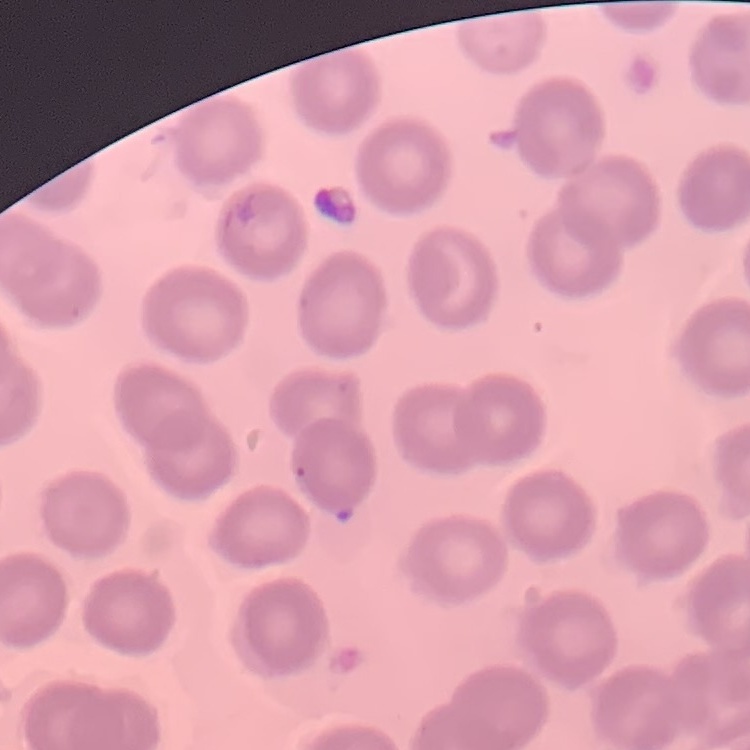
red blood cell morphology = no rouleaux formation
preparation = thin blood smear
image type = one tile cut from a larger photomicrograph
stain = Field's or Giemsa